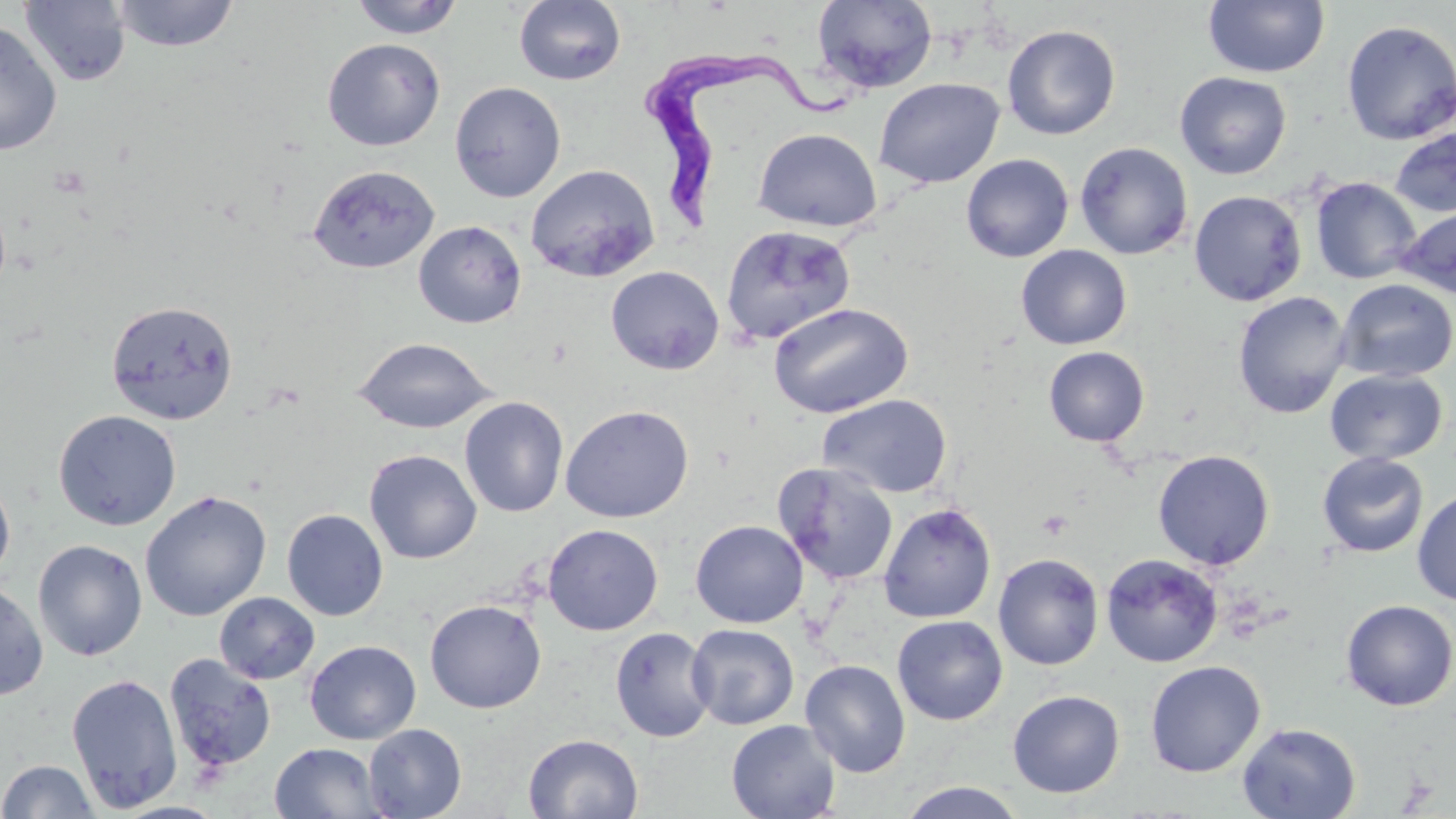

Summary:
  - Coordinate format: approximate bounding boxes as [x1, y1, x2, y2] in pixels
  - Uninfected red blood cell locations: [349, 0, 465, 39], [513, 0, 626, 86], [1203, 0, 1330, 79], [20, 1, 131, 86], [109, 1, 240, 52], [811, 1, 938, 93], [0, 19, 62, 157], [1341, 20, 1456, 145], [1002, 24, 1120, 140], [322, 38, 445, 151], [1174, 72, 1292, 180], [873, 77, 1005, 189], [449, 80, 566, 202], [752, 127, 882, 232], [1390, 128, 1456, 218], [1075, 142, 1194, 260], [961, 153, 1073, 262], [525, 163, 660, 282], [308, 164, 439, 274], [1310, 177, 1422, 285], [1189, 190, 1307, 306], [1394, 203, 1456, 299], [413, 220, 527, 328], [720, 223, 855, 346], [1015, 245, 1132, 350], [606, 265, 724, 375], [1335, 279, 1456, 383], [1232, 291, 1352, 419], [106, 299, 239, 425], [768, 302, 914, 418], [353, 337, 497, 434], [1043, 346, 1150, 446], [1324, 369, 1447, 465], [818, 394, 953, 498], [459, 396, 569, 518], [560, 404, 694, 523], [53, 409, 182, 530], [364, 449, 482, 564], [1153, 449, 1275, 570], [1317, 452, 1429, 558], [773, 462, 899, 585], [0, 472, 15, 588], [1412, 488, 1456, 606], [139, 490, 272, 621], [878, 502, 996, 623], [282, 508, 388, 621], [690, 519, 808, 628], [542, 524, 664, 636], [33, 539, 147, 662], [992, 553, 1105, 670], [1101, 554, 1223, 667], [0, 582, 49, 701], [214, 592, 320, 684], [1340, 599, 1455, 711], [425, 600, 546, 713], [892, 615, 1008, 725], [687, 623, 798, 730], [610, 626, 716, 743], [304, 640, 421, 745], [164, 653, 277, 774], [800, 659, 911, 777], [1145, 660, 1266, 777], [66, 671, 183, 812], [1008, 690, 1125, 798], [725, 719, 842, 819], [1237, 721, 1361, 818], [363, 724, 466, 818], [524, 732, 644, 819], [269, 742, 387, 819], [0, 759, 100, 818], [898, 781, 1026, 818]
  - Trypanosoma brucei locations: [642, 49, 853, 235]
  - Platelet locations: [1036, 509, 1072, 540]
  - Slide-level diagnosis: Trypanosoma brucei
  - Modality: optical microscopy
  - Field of view: one of a larger specimen
  - Preparation: thin blood smear
  - Image size: 1456×819 pixels
  - Magnification: 1000x
  - Stain: May-Grünwald-Giemsa